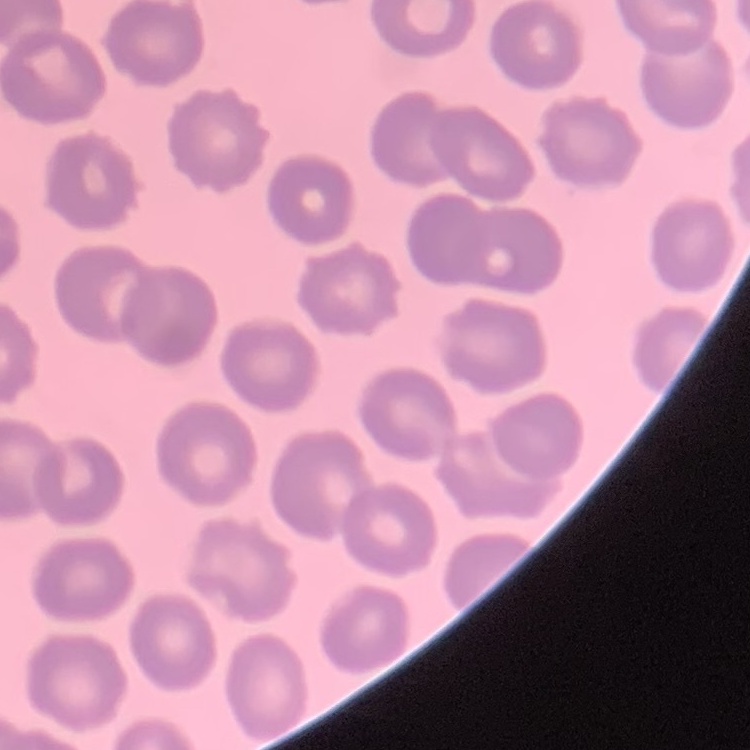

Summary:
  - Red blood cell morphology: no rouleaux formation
  - Stain: Field's or Giemsa
  - Image type: square crop of a larger photomicrograph
  - Preparation: thin blood smear